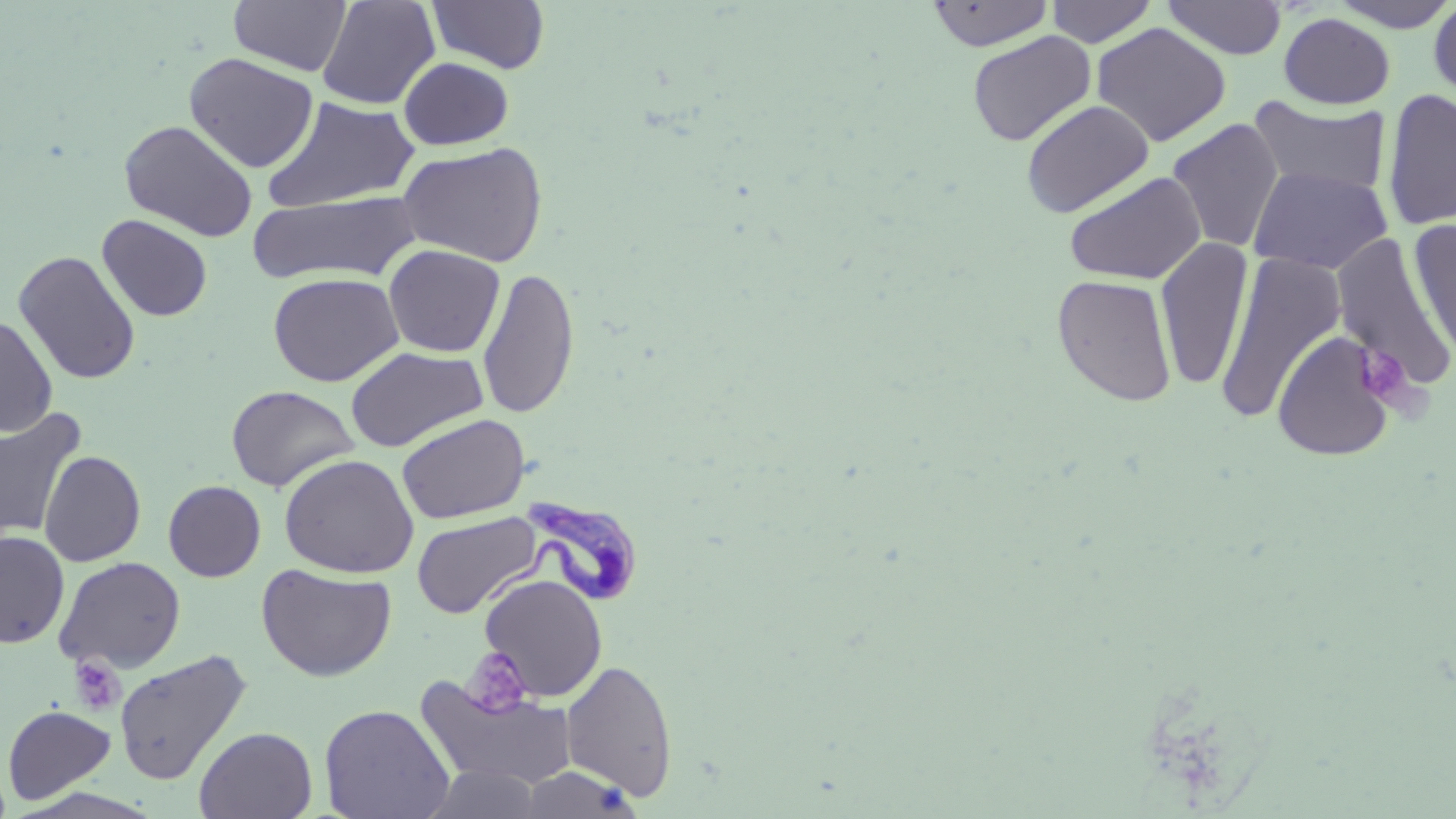

Summary:
  - Coordinate format: approximate bounding boxes as named x1/y1/x2/y2 corners in pixels
  - Trypanosoma brucei locations: (x1=517, y1=493, x2=648, y2=608)
  - Platelet locations: (x1=1355, y1=346, x2=1415, y2=407), (x1=462, y1=647, x2=533, y2=716), (x1=68, y1=656, x2=126, y2=715)
  - Uninfected red blood cell locations: (x1=229, y1=0, x2=352, y2=76), (x1=316, y1=0, x2=440, y2=110), (x1=1046, y1=0, x2=1158, y2=47), (x1=1327, y1=0, x2=1456, y2=33), (x1=1428, y1=0, x2=1456, y2=104), (x1=427, y1=1, x2=550, y2=74), (x1=925, y1=1, x2=1055, y2=52), (x1=1162, y1=1, x2=1287, y2=60), (x1=1279, y1=13, x2=1395, y2=109), (x1=1091, y1=22, x2=1232, y2=147), (x1=967, y1=31, x2=1096, y2=146), (x1=184, y1=52, x2=319, y2=173), (x1=398, y1=57, x2=514, y2=150), (x1=1382, y1=87, x2=1456, y2=233), (x1=1248, y1=95, x2=1392, y2=197), (x1=262, y1=96, x2=421, y2=214), (x1=1021, y1=99, x2=1155, y2=217), (x1=1166, y1=118, x2=1284, y2=255), (x1=118, y1=119, x2=257, y2=241), (x1=396, y1=141, x2=549, y2=268), (x1=1248, y1=165, x2=1393, y2=275), (x1=1063, y1=171, x2=1207, y2=285), (x1=248, y1=191, x2=423, y2=285), (x1=97, y1=214, x2=213, y2=322), (x1=1408, y1=219, x2=1455, y2=366), (x1=1332, y1=233, x2=1453, y2=392), (x1=1155, y1=237, x2=1254, y2=391), (x1=383, y1=244, x2=505, y2=357), (x1=13, y1=250, x2=141, y2=385), (x1=1215, y1=253, x2=1347, y2=424), (x1=478, y1=267, x2=580, y2=420), (x1=268, y1=272, x2=403, y2=387), (x1=1052, y1=274, x2=1177, y2=406), (x1=0, y1=315, x2=58, y2=436), (x1=1272, y1=329, x2=1397, y2=462), (x1=345, y1=346, x2=488, y2=452), (x1=226, y1=385, x2=358, y2=493), (x1=0, y1=408, x2=87, y2=540), (x1=396, y1=413, x2=530, y2=524), (x1=39, y1=450, x2=146, y2=567), (x1=278, y1=454, x2=418, y2=578), (x1=163, y1=480, x2=266, y2=582), (x1=412, y1=512, x2=541, y2=619), (x1=0, y1=531, x2=70, y2=649), (x1=54, y1=556, x2=186, y2=673), (x1=256, y1=563, x2=397, y2=682), (x1=479, y1=574, x2=607, y2=701), (x1=114, y1=649, x2=252, y2=785), (x1=561, y1=658, x2=678, y2=802), (x1=415, y1=675, x2=579, y2=791), (x1=318, y1=703, x2=455, y2=818), (x1=2, y1=705, x2=116, y2=805), (x1=194, y1=726, x2=316, y2=819), (x1=420, y1=765, x2=544, y2=818), (x1=516, y1=765, x2=644, y2=817)
  - Slide-level diagnosis: Trypanosoma brucei
  - Magnification: 1000x
  - Modality: optical microscopy
  - Image size: 1456×819 pixels
  - Stain: May-Grünwald-Giemsa
  - Field of view: one of a larger specimen
  - Preparation: thin blood film